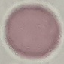

Summary:
  - Malaria status: uninfected
  - Capture: smartphone through the microscope eyepiece
  - Image type: cell patch, automatically extracted from a larger field of view and resized to 64 × 64 pixels
  - Stain: Giemsa
  - Preparation: thin blood film